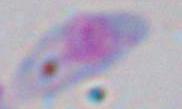
Summary:
  - Identification: Toxoplasma gondii
  - Magnification: 1000x
  - Modality: photomicrograph